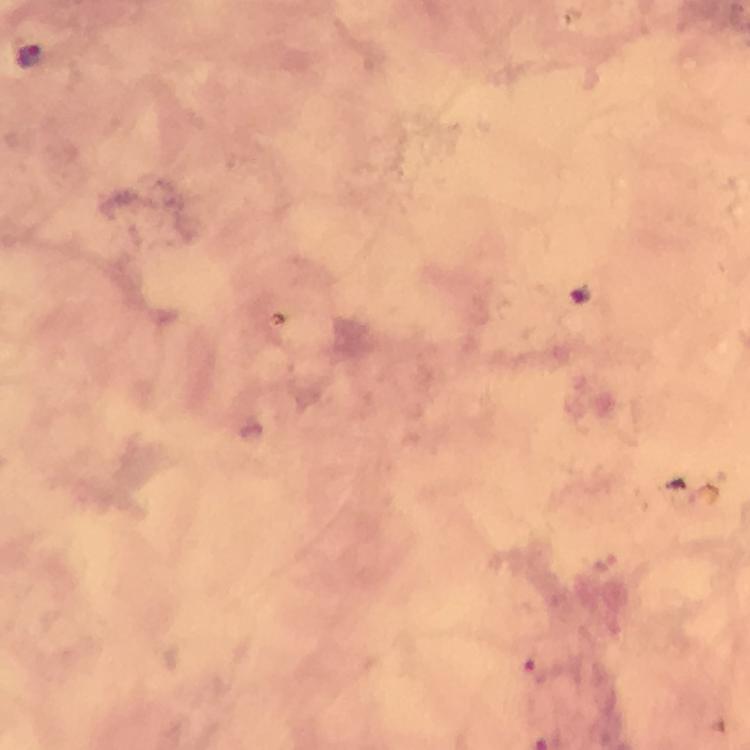

Approximate object centers, in pixels from the top-left corner. Plasmodium parasite locations: (x=29, y=57). Giemsa-stained preparation. 100x magnification. From a diagnostic examination for malaria. Image is 750×750 pixels. Immersion oil was used. A crop from one field of view. Thick smear. Photographed through the microscope with a smartphone camera.